Name the parasite shown.
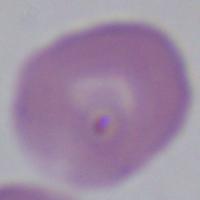

This is Babesia.

magnification = 1000x
modality = micrograph